Locate and identify every blood parasite.
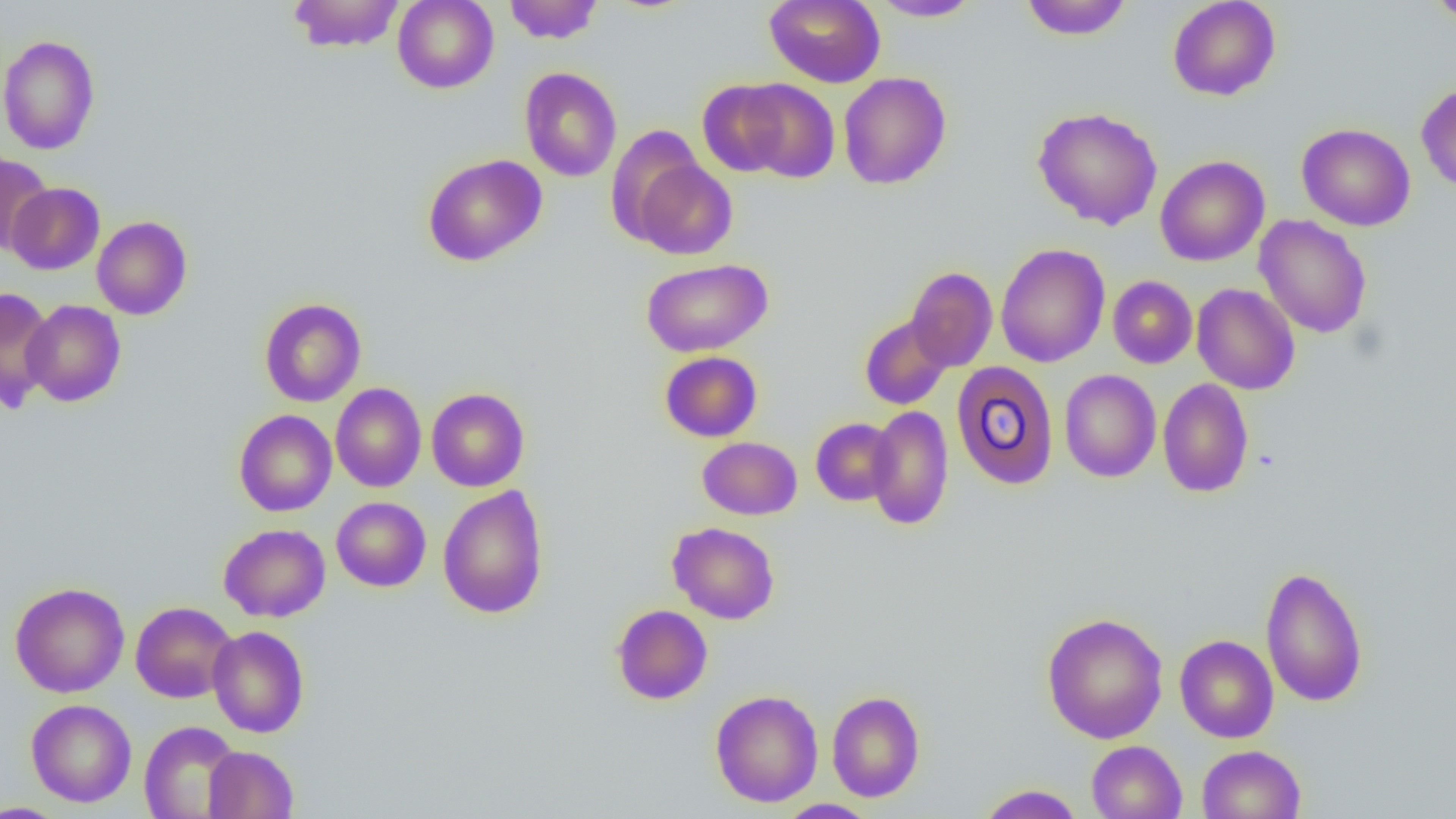

No blood parasites seen.

Approximate bounding boxes as (x1, y1, x2, y2) in pixels. Uninfected red blood cell locations: (287, 0, 405, 53), (392, 0, 499, 93), (503, 0, 603, 44), (764, 0, 885, 88), (871, 0, 983, 21), (1020, 0, 1133, 40), (1168, 0, 1281, 101), (1429, 0, 1456, 25), (0, 34, 100, 155), (519, 67, 622, 182), (838, 71, 951, 190), (736, 78, 841, 183), (698, 79, 795, 177), (1416, 83, 1456, 193), (1032, 106, 1163, 230), (1297, 123, 1416, 231), (605, 126, 706, 245), (0, 153, 53, 257), (422, 153, 547, 266), (1155, 155, 1269, 266), (632, 159, 737, 259), (6, 181, 105, 275), (1254, 215, 1372, 338), (92, 216, 192, 320), (995, 243, 1110, 367), (641, 258, 773, 357), (906, 267, 998, 372), (1108, 275, 1197, 368), (1192, 283, 1300, 394), (0, 287, 56, 411), (259, 298, 366, 407), (22, 300, 126, 407), (859, 314, 953, 410), (659, 351, 762, 442), (952, 361, 1059, 490), (1059, 369, 1161, 483), (1157, 378, 1254, 498), (330, 383, 427, 492), (426, 387, 529, 492), (866, 406, 954, 530), (234, 409, 337, 517), (811, 418, 898, 505), (698, 437, 802, 519), (437, 485, 549, 619), (331, 497, 431, 592), (667, 522, 780, 624), (218, 524, 331, 622), (1260, 565, 1369, 708), (10, 581, 129, 697), (130, 601, 237, 703), (611, 604, 713, 705), (1041, 612, 1168, 744), (208, 626, 309, 737), (1175, 634, 1278, 742), (710, 689, 823, 807), (826, 691, 926, 802), (26, 699, 136, 807), (139, 720, 242, 818), (1086, 740, 1187, 819), (1197, 744, 1306, 819), (203, 745, 298, 818), (977, 784, 1084, 819), (776, 799, 879, 819), (0, 802, 69, 818). Slide-level diagnosis: negative for blood parasites. Optical microscopy. 1000x magnification. Image is 1456×819 pixels. Thin blood film. Single field of view.